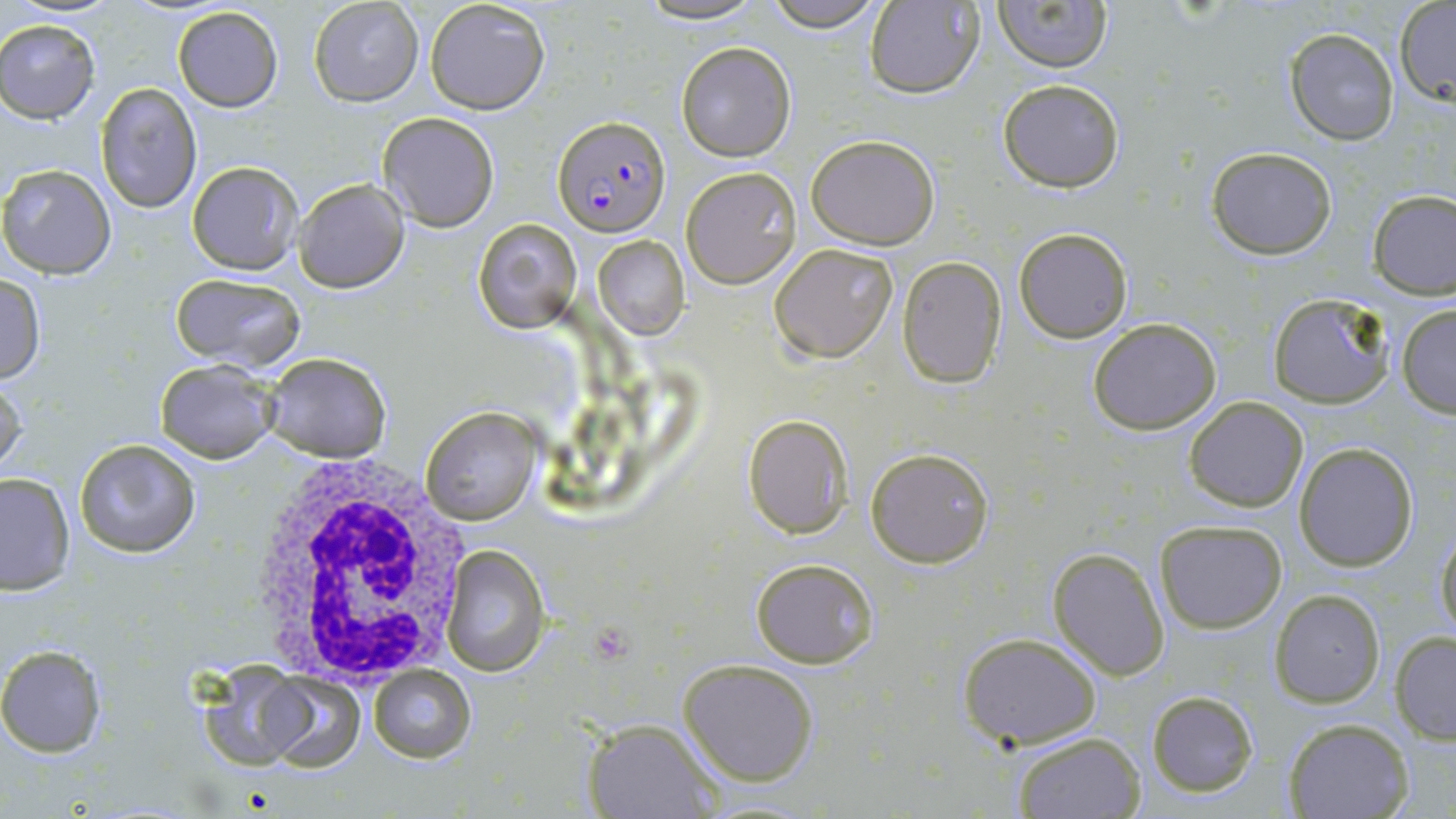

Approximate bounding boxes as [x1, y1, x2, y2] in pixels. Uninfected red blood cell locations: [309, 0, 423, 107], [424, 0, 551, 115], [633, 0, 770, 26], [763, 0, 890, 31], [993, 0, 1112, 72], [865, 1, 984, 99], [1395, 2, 1456, 102], [172, 6, 283, 111], [1, 18, 100, 121], [1284, 28, 1400, 144], [676, 41, 796, 162], [997, 79, 1125, 190], [96, 81, 202, 214], [377, 112, 500, 231], [805, 133, 941, 249], [1206, 146, 1340, 260], [187, 161, 302, 275], [1, 163, 118, 278], [680, 166, 802, 289], [294, 179, 408, 293], [1368, 189, 1455, 298], [474, 217, 581, 334], [1014, 227, 1132, 343], [593, 235, 688, 339], [769, 242, 899, 364], [897, 256, 1007, 389], [0, 271, 45, 385], [171, 274, 306, 370], [1266, 293, 1396, 410], [1396, 304, 1456, 417], [1087, 317, 1223, 435], [261, 351, 391, 460], [154, 360, 279, 463], [0, 376, 27, 481], [1183, 395, 1308, 512], [420, 405, 543, 528], [742, 414, 853, 539], [72, 437, 202, 556], [1293, 442, 1419, 571], [865, 446, 994, 568], [0, 472, 75, 596], [1155, 519, 1287, 633], [1434, 519, 1456, 646], [439, 545, 550, 677], [1047, 547, 1171, 680], [749, 557, 879, 668], [1270, 590, 1386, 708], [1390, 631, 1456, 744], [957, 633, 1102, 749], [0, 645, 107, 756], [678, 657, 821, 786], [193, 663, 317, 774], [368, 667, 475, 763], [262, 673, 364, 773], [1146, 689, 1259, 797], [581, 717, 720, 819], [1282, 718, 1413, 819], [1011, 732, 1145, 818]. White blood cell locations: [246, 455, 474, 680]. Plasmodium falciparum-infected red blood cell locations: [553, 116, 671, 238]. Slide-level diagnosis: Plasmodium falciparum. Light microscopy. Thin blood smear. 1000x magnification. Single field of view. May-Grünwald-Giemsa stain. Image is 1456×819 pixels.